Classify this cell by malaria status.
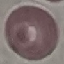
It is uninfected.

Giemsa-stained preparation. Acquired by smartphone through the microscope eyepiece. Thin blood smear. Automatically extracted cell patch, resized to 64 × 64 pixels.